Comment on the morphology of the red blood cells.
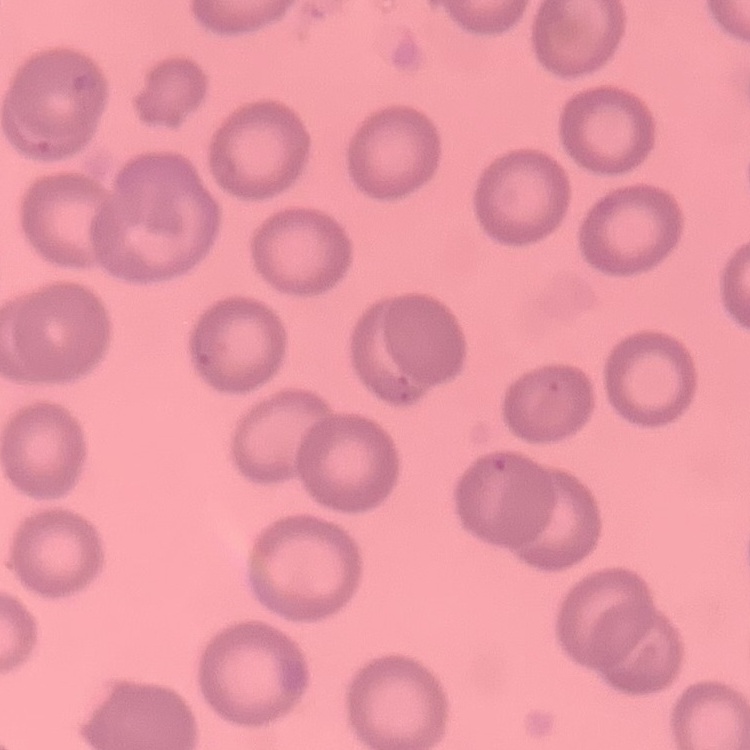
No rouleaux formation.

Summary:
  - Stain: Field's or Giemsa
  - Preparation: thin peripheral smear
  - Image type: one tile cut from a larger photomicrograph